Identify the cell.
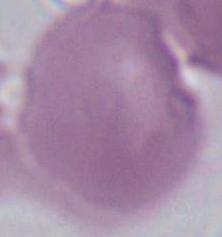
An erythrocyte.

Captured at 1000x magnification. Micrograph.